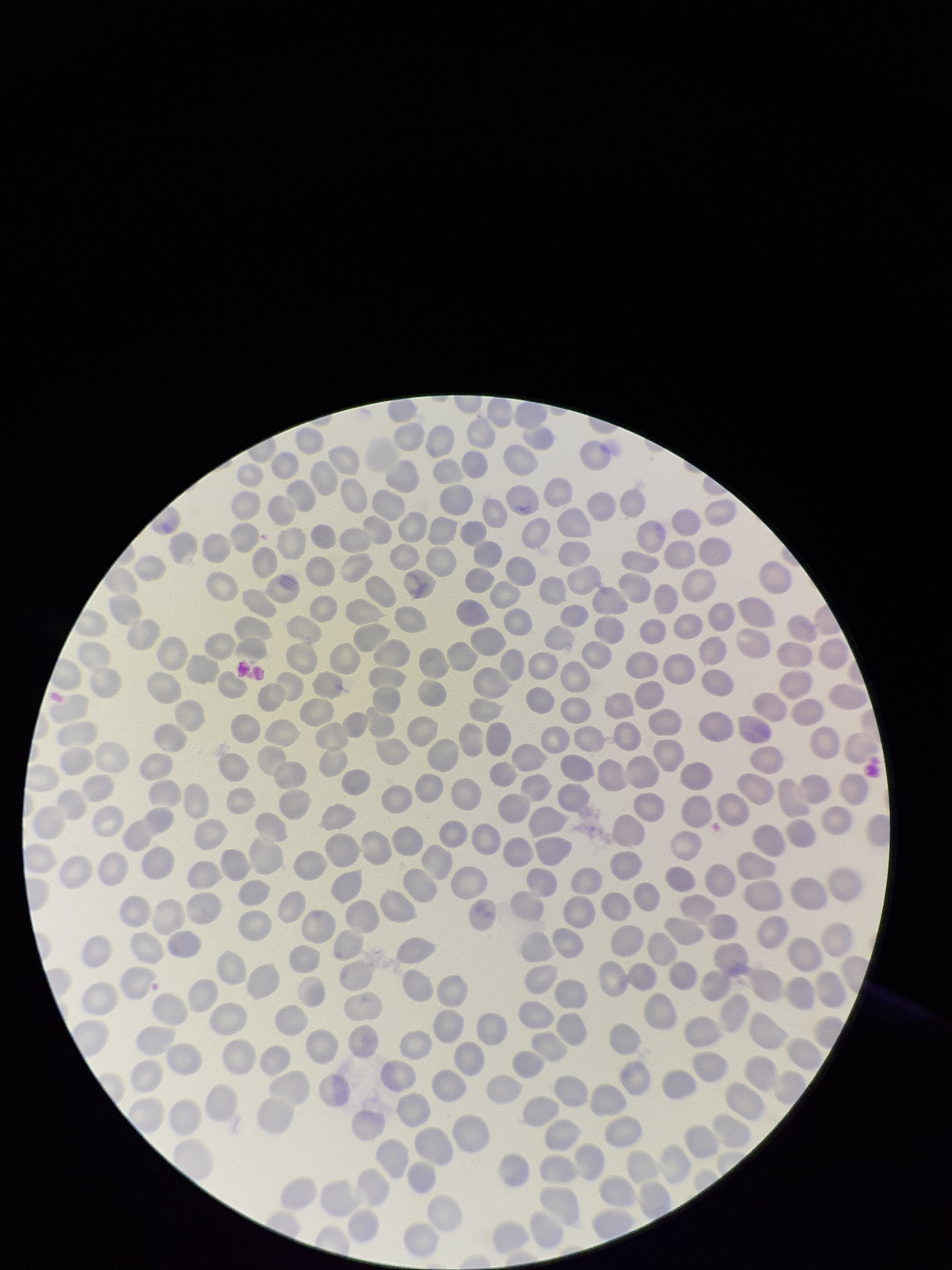
Summary:
  - Parasitized red blood cell count: 0
  - Preparation: thin
  - Field of view: single
  - Stain: Giemsa
  - Red blood cell count: 311
  - Image size: 952×1270 pixels
  - Parasitized red blood cells: none seen
  - Patient malaria status: negative
  - Capture: smartphone photograph through the microscope eyepiece